Report the malaria status of this cell.
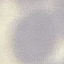
Uninfected.

Summary:
  - Capture: smartphone camera at the microscope eyepiece
  - Stain: Giemsa
  - Image type: automatically extracted cell patch, resized to 64 × 64 pixels
  - Preparation: thin blood smear